Report the malaria status of this cell.
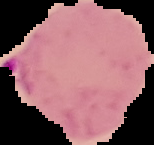
Parasitized.

image type = cell region segmented out of the field of view; surrounding area masked to black
preparation = thin blood film
image size = 154×145 pixels